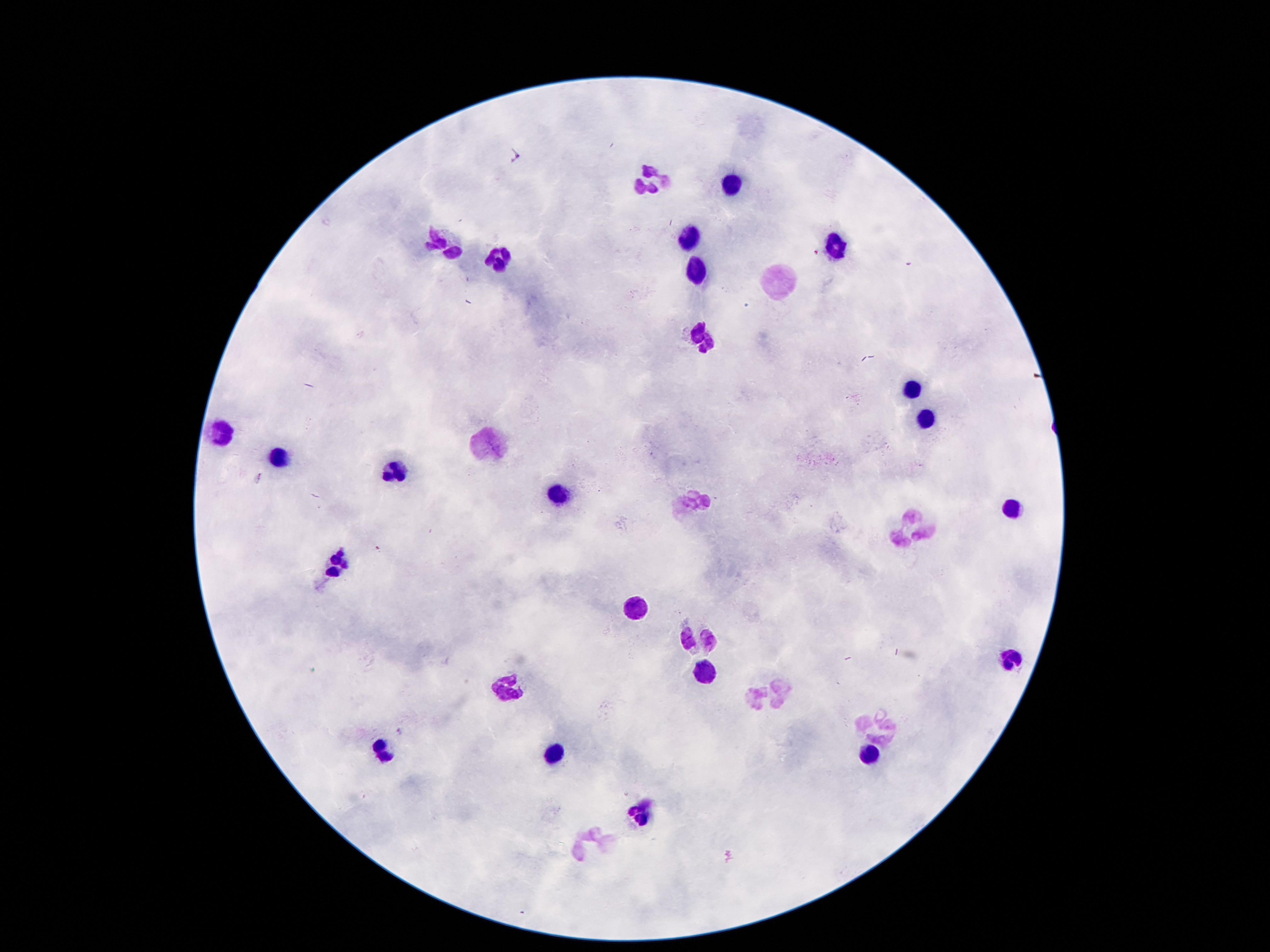 Approximate centers as [x, y] in pixels. Leukocyte locations: [649, 179], [732, 182], [691, 241], [442, 243], [836, 247], [498, 262], [698, 274], [776, 284], [702, 338], [914, 386], [923, 419], [221, 432], [486, 443], [282, 457], [396, 468], [561, 497], [694, 502], [1013, 511], [914, 529], [333, 564], [633, 607], [696, 639], [1011, 659], [706, 668], [509, 684], [773, 693], [880, 723], [381, 749], [553, 753], [870, 756], [639, 818], [599, 841]. Giemsa-stained preparation. Image is 1270×952 pixels. Single field of view. Photographed through the microscope eyepiece with a smartphone camera. Thick blood film. 100x magnification. Patient malaria status: uninfected.